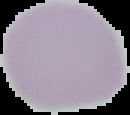
Image is 130×115 pixels. Result: no malaria parasites seen. Cell region segmented out of the field of view; the surrounding area is masked to black. From a thin blood film.